Comment on the morphology of the red blood cells.
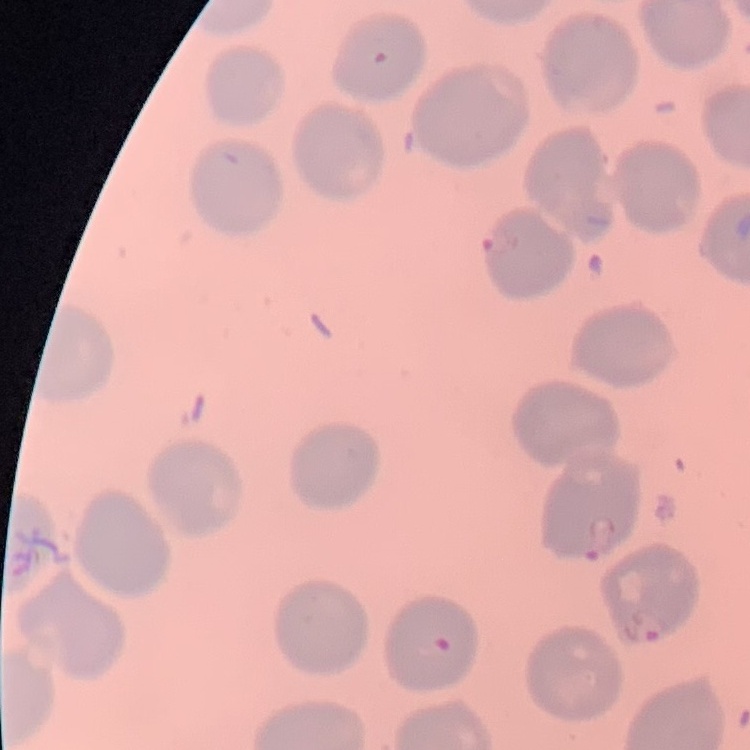
No rouleaux formation.

Summary:
  - Stain: Field's or Giemsa
  - Image type: square crop of a larger photomicrograph
  - Preparation: thin peripheral smear